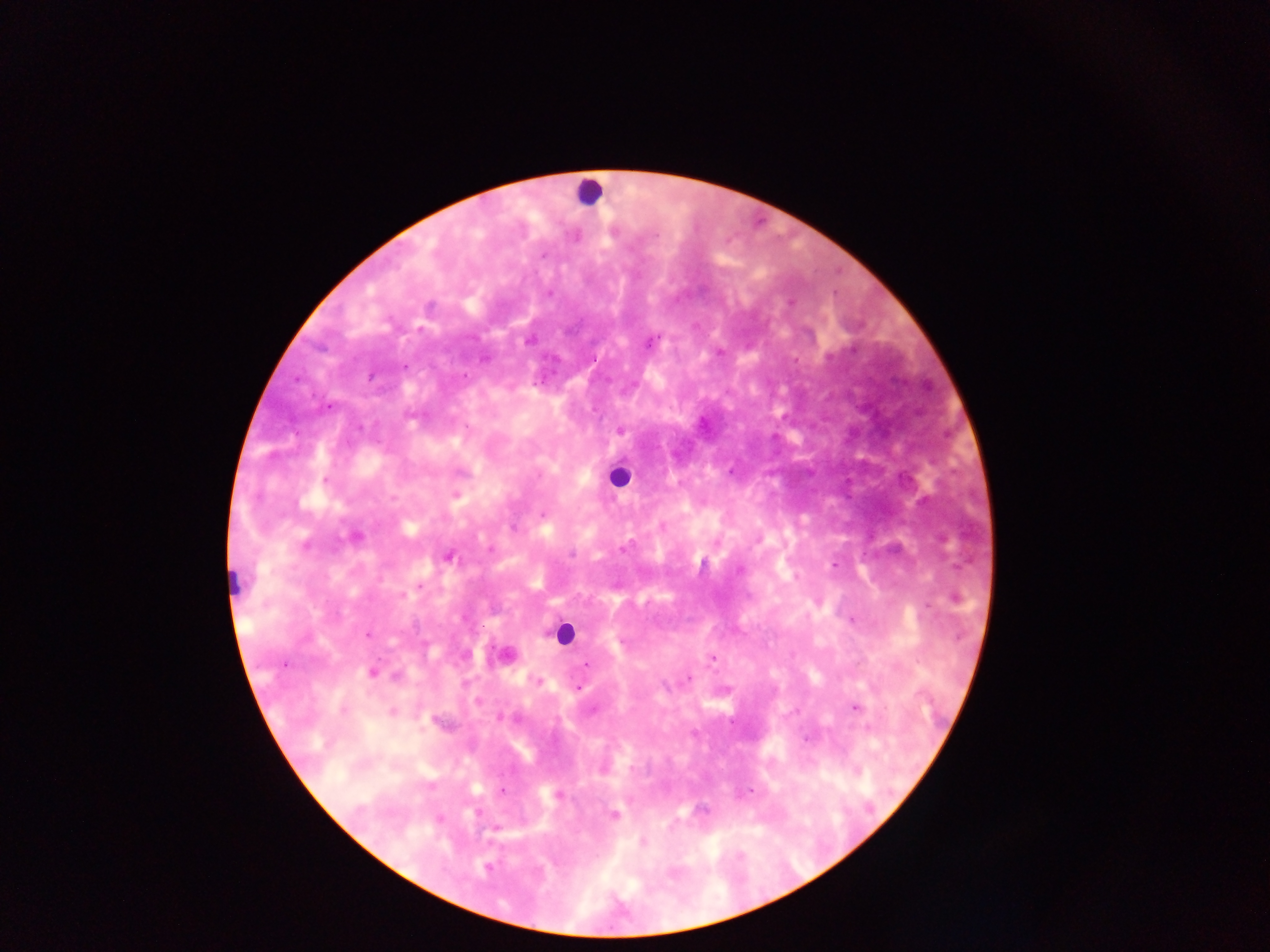 Approximate centers as x y in pixels. Malaria parasite locations: 656 235; 543 256; 550 293; 791 302; 527 341; 650 342; 829 358; 485 359; 405 366; 371 377; 329 407; 467 426; 360 427; 621 431; 325 480; 455 494; 306 545; 622 548; 490 549; 572 554; 448 557; 834 564; 420 586; 401 596; 956 598; 852 620; 368 634; 622 640; 713 658; 586 664; 284 665; 371 673; 395 676; 688 679; 537 681; 579 688; 855 707; 393 712; 499 718; 502 791; 751 791; 558 795; 702 810; 614 815; 439 819; 643 842; 487 868; 673 874. Leukocyte locations: 589 192; 618 475; 564 634. Single field of view. Sample from Ghana. Mobile-phone photograph taken through the microscope. Image is 1270×952 pixels. Thick blood smear.